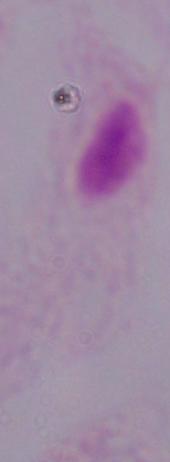

identification: trichomonad
modality: photomicrograph
magnification: 1000x